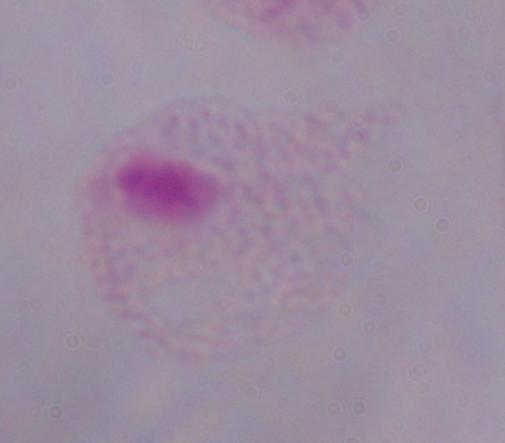
A trichomonad is seen. 1000x magnification. Micrograph.